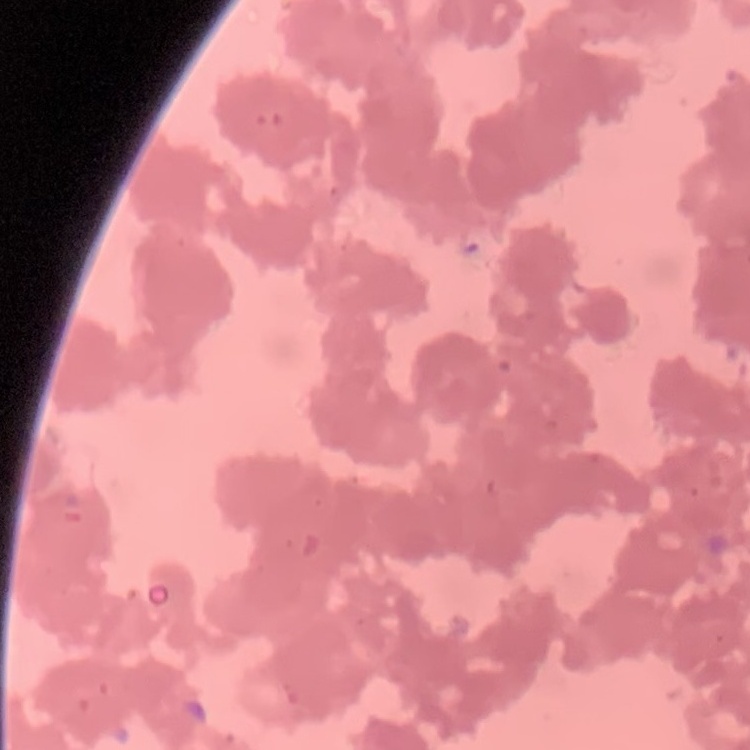

The erythrocytes show rouleaux formation. One tile cut from a larger photomicrograph. Stained with either Field's or Giemsa. Thin peripheral smear.